Point out each Plasmodium parasite.
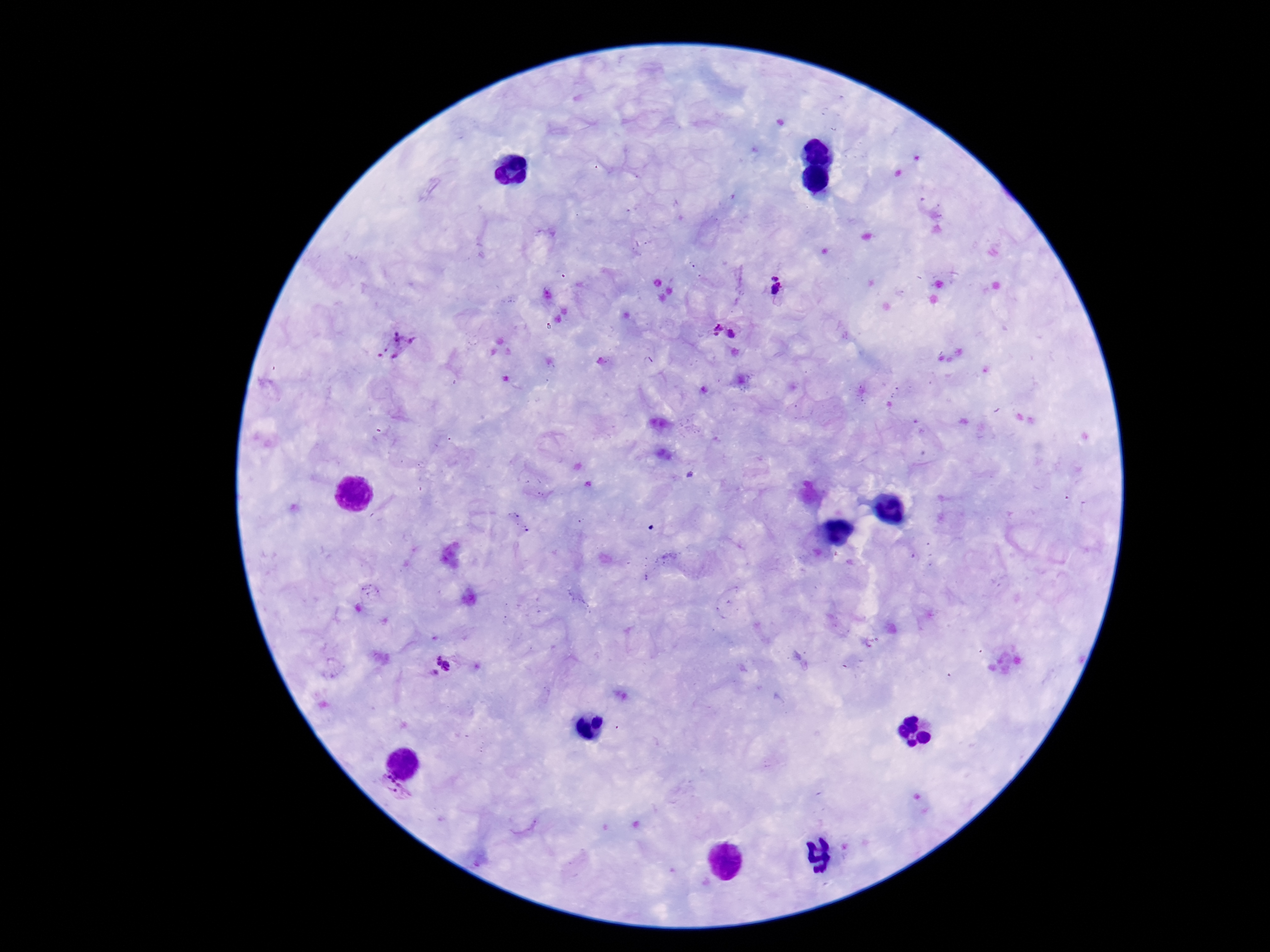
Approximate centers as (x, y) in pixels.
Plasmodium parasites: (776, 285), (713, 330), (732, 333), (396, 344), (443, 666), (395, 788).

Image is 1270×952 pixels. 100x magnification. Thick peripheral-blood smear. Giemsa stain. Single field of view. Patient malaria status: infected. Smartphone photograph taken through the microscope eyepiece.